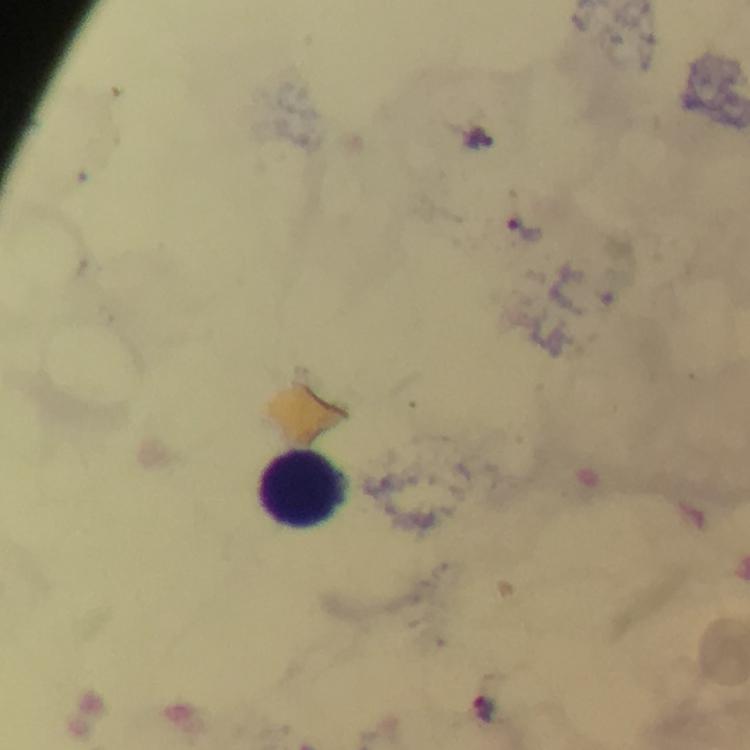

{
  "leukocyte_locations": "approximate object centers, in pixels from the top-left corner: (x=303, y=487)",
  "stain": "Giemsa",
  "image_size": "750×750 pixels",
  "plasmodium_parasite_locations": "approximate object centers, in pixels from the top-left corner: (x=478, y=140), (x=524, y=229), (x=480, y=711)",
  "context": "from a diagnostic examination for malaria",
  "capture": "smartphone mounted on the microscope",
  "magnification": "100x",
  "immersion_oil": "applied",
  "preparation": "thick blood smear",
  "cropped_from": "a single field of view"
}